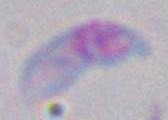
1000x magnification. Toxoplasma gondii is seen. Micrograph.